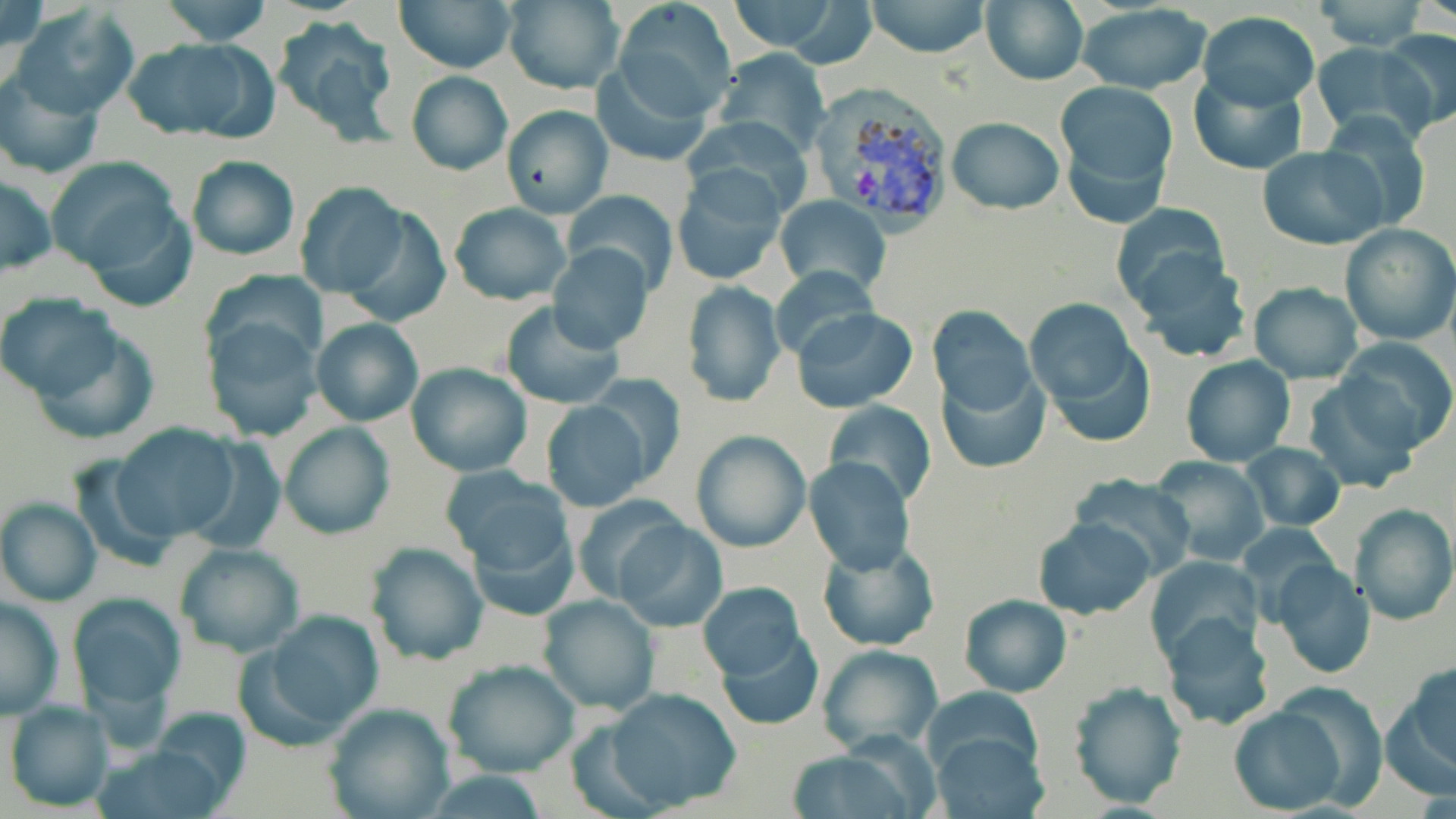
Approximate bounding boxes as (x1, y1, x2, y2) in pixels. Uninfected red blood cell locations: (0, 0, 48, 83), (161, 0, 271, 47), (394, 0, 517, 73), (725, 0, 851, 55), (865, 0, 991, 58), (1308, 0, 1430, 50), (501, 1, 624, 93), (979, 1, 1089, 85), (613, 3, 733, 121), (8, 5, 140, 120), (1074, 5, 1214, 93), (1196, 11, 1320, 109), (272, 15, 401, 144), (1378, 29, 1456, 132), (122, 37, 273, 143), (1309, 41, 1434, 145), (711, 49, 831, 158), (589, 59, 714, 167), (0, 71, 105, 179), (406, 71, 513, 175), (1188, 72, 1306, 175), (1054, 80, 1177, 226), (501, 104, 612, 218), (685, 115, 813, 221), (1316, 115, 1433, 234), (947, 116, 1064, 214), (1258, 146, 1386, 250), (186, 155, 299, 262), (45, 156, 186, 287), (673, 170, 787, 288), (1, 174, 56, 277), (297, 184, 410, 301), (561, 191, 679, 295), (80, 192, 199, 315), (774, 196, 890, 298), (449, 201, 572, 306), (1111, 201, 1233, 310), (340, 206, 452, 329), (1340, 223, 1455, 346), (546, 242, 655, 353), (1126, 248, 1253, 364), (770, 266, 883, 366), (202, 271, 327, 371), (681, 282, 785, 407), (1247, 282, 1364, 384), (2, 295, 121, 403), (1025, 298, 1144, 412), (501, 302, 625, 410), (931, 306, 1036, 413), (791, 307, 919, 413), (204, 314, 322, 442), (24, 317, 160, 446), (311, 318, 423, 426), (1337, 336, 1456, 454), (1180, 356, 1295, 467), (405, 362, 533, 477), (937, 363, 1051, 475), (586, 375, 686, 483), (1301, 379, 1423, 493), (540, 400, 652, 513), (824, 401, 935, 503), (277, 420, 396, 540), (110, 423, 239, 544), (691, 431, 811, 553), (1239, 441, 1346, 531), (67, 455, 182, 573), (1150, 455, 1269, 567), (806, 459, 915, 574), (444, 470, 575, 597), (1069, 472, 1197, 576), (571, 492, 690, 604), (0, 498, 100, 606), (1349, 502, 1456, 626), (1032, 517, 1157, 620), (611, 519, 727, 631), (1237, 522, 1341, 625), (816, 539, 938, 651), (174, 542, 305, 658), (366, 542, 487, 665), (1145, 554, 1261, 661), (1271, 560, 1375, 678), (696, 582, 807, 690), (67, 593, 186, 722), (538, 594, 660, 714), (958, 594, 1072, 697), (0, 597, 62, 718), (253, 610, 386, 739), (1159, 611, 1276, 731), (714, 625, 824, 731), (816, 644, 943, 755), (442, 658, 580, 779), (1385, 661, 1456, 795), (1066, 681, 1188, 809), (1271, 683, 1390, 810), (924, 686, 1043, 777), (603, 687, 744, 813), (5, 698, 116, 812), (322, 702, 455, 819), (1227, 706, 1345, 814), (144, 707, 254, 811), (933, 732, 1048, 818), (94, 744, 231, 819), (789, 751, 920, 819). Plasmodium vivax-infected red blood cell locations: (808, 88, 956, 227). Slide-level diagnosis: Plasmodium vivax. May-Grünwald-Giemsa stain. Image is 1456×819 pixels. Optical microscopy. Thin blood film. 1000x magnification. Single field of view.